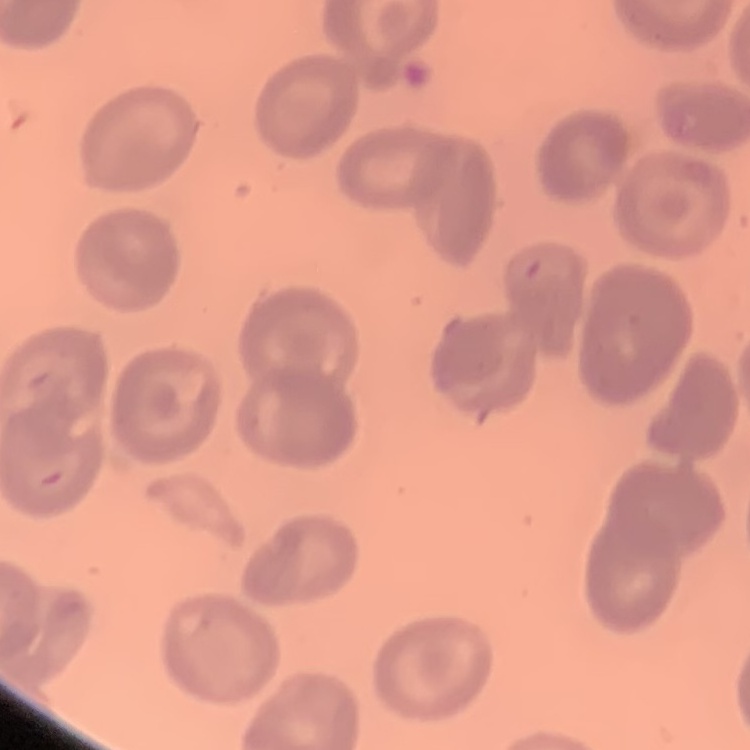

Summary:
  - Erythrocyte morphology: no rouleaux formation
  - Stain: Field's or Giemsa
  - Preparation: thin blood smear
  - Image type: square crop of a larger photomicrograph